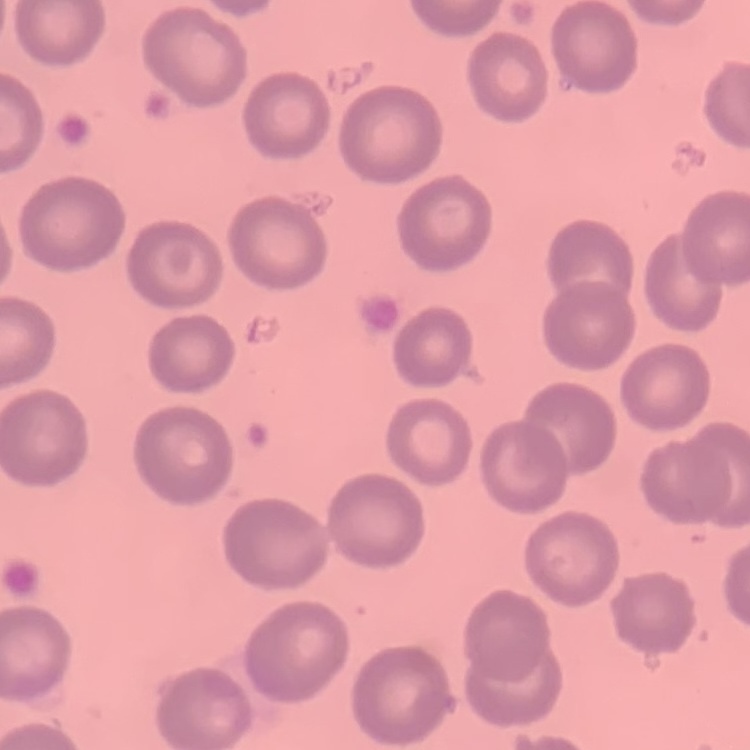

erythrocyte morphology = no rouleaux formation
stain = Field's or Giemsa
preparation = thin peripheral smear
image type = one tile cut from a larger photomicrograph